Assess the morphology of the erythrocytes.
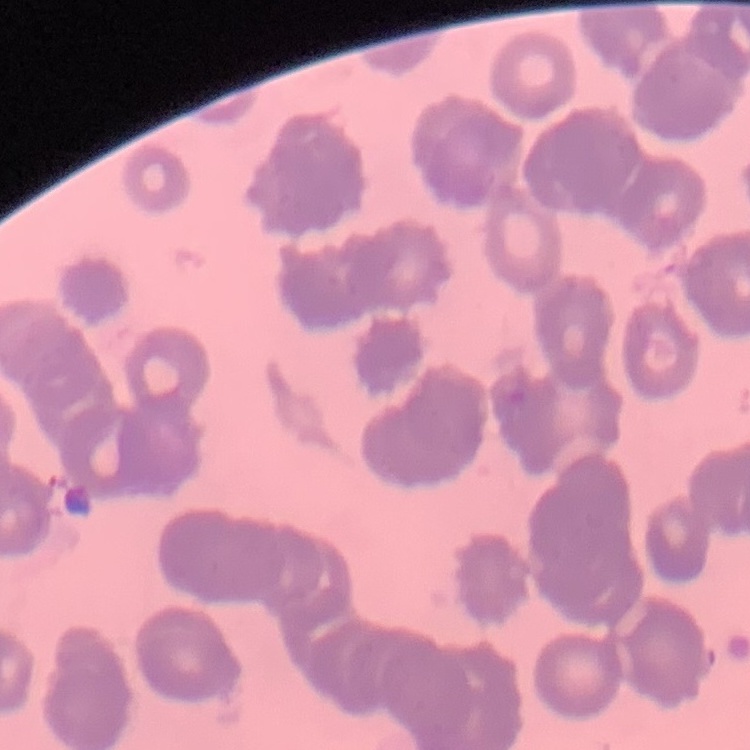

Rouleaux formation.

One tile cut from a larger photomicrograph. Thin blood film. Field's or Giemsa stain.